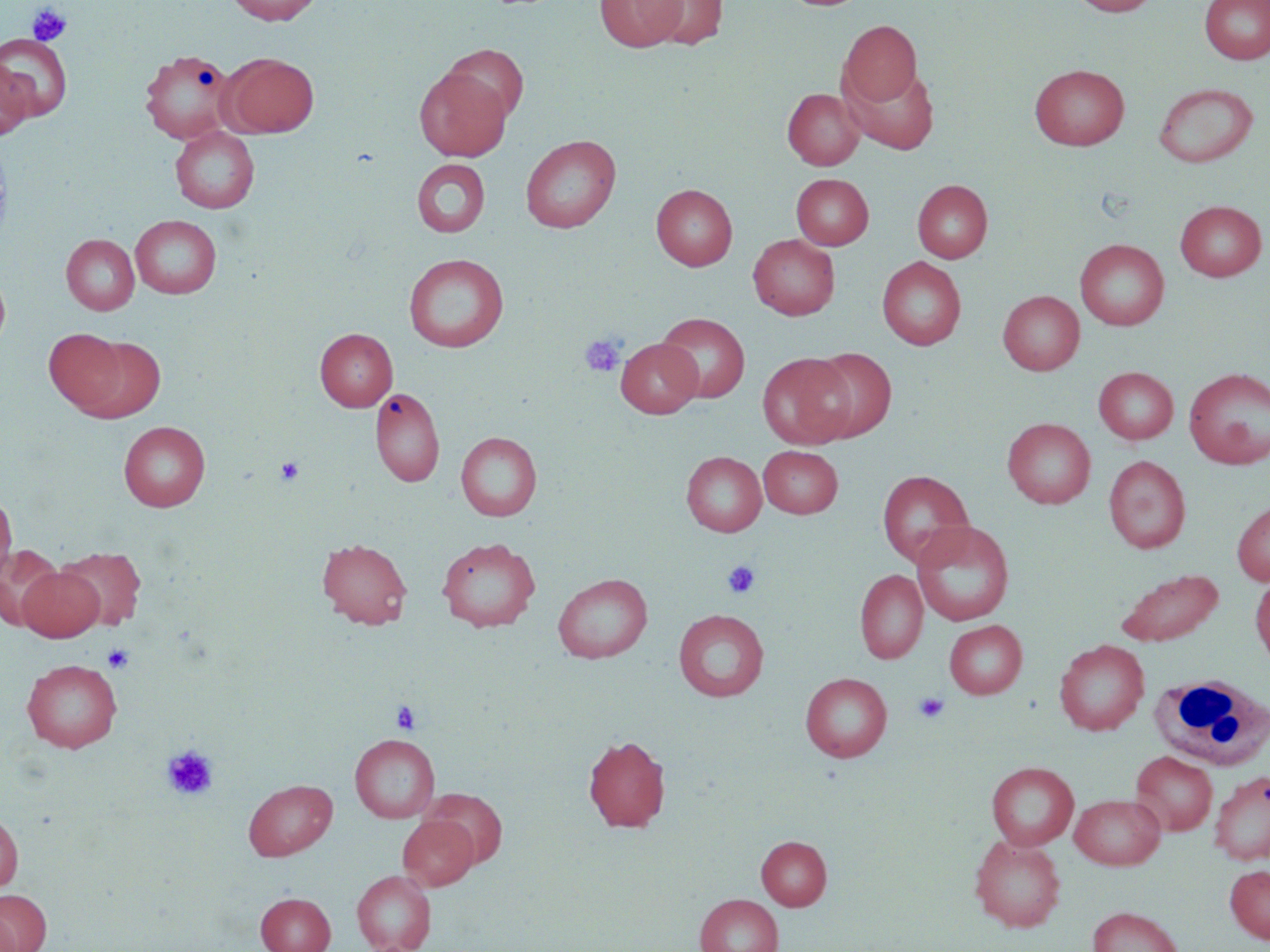

{
  "slide_level_diagnosis": "no evidence of blood parasites",
  "platelet_locations": "approximate bounding boxes as (x1,y1)-(x2,y2) corner pairs in pixels: (27,3)-(71,46), (580,334)-(626,377), (275,457)-(306,485), (722,560)-(761,599), (102,644)-(135,674), (913,692)-(949,724), (391,700)-(421,735), (161,745)-(219,801)",
  "field_of_view": "single",
  "uninfected_red_blood_cell_locations": "approximate bounding boxes as (x1,y1)-(x2,y2) corner pairs in pixels: (226,0)-(323,25), (643,0)-(728,49), (1068,0)-(1160,16), (1200,0)-(1270,64), (596,1)-(685,51), (838,19)-(922,110), (0,34)-(73,120), (442,43)-(529,124), (139,49)-(236,145), (221,53)-(319,137), (0,60)-(34,140), (1029,64)-(1129,151), (843,65)-(940,155), (414,67)-(511,161), (1154,82)-(1258,167), (783,88)-(864,170), (170,127)-(259,213), (520,134)-(621,233), (411,159)-(490,237), (791,174)-(874,249), (912,179)-(993,263), (651,184)-(737,271), (1175,200)-(1267,281), (130,215)-(222,299), (61,233)-(140,315), (748,234)-(840,320), (1074,238)-(1170,330), (403,253)-(509,352), (877,256)-(966,350), (0,269)-(11,353), (998,290)-(1084,375), (656,313)-(750,403), (45,327)-(127,415), (315,327)-(397,411), (77,336)-(166,422), (615,338)-(702,418), (808,347)-(897,442), (758,352)-(855,448), (1093,366)-(1178,444), (1183,368)-(1270,469), (370,386)-(445,487), (1002,417)-(1095,508), (119,421)-(209,511), (455,431)-(542,521), (758,446)-(843,518), (680,451)-(767,536), (1104,455)-(1190,553), (877,470)-(973,568), (0,491)-(17,583), (1232,500)-(1270,586), (911,520)-(1015,626), (436,537)-(541,632), (317,538)-(413,629), (0,546)-(65,629), (55,546)-(146,630), (18,565)-(104,641), (1115,568)-(1224,647), (855,569)-(928,664), (552,573)-(653,663), (1250,574)-(1270,667), (673,609)-(769,701), (944,620)-(1027,699), (1054,639)-(1149,735), (22,659)-(122,752), (800,672)-(892,762), (349,734)-(440,822), (583,734)-(670,832), (1130,750)-(1218,835), (986,761)-(1079,850), (1209,770)-(1270,865), (243,779)-(337,860), (421,788)-(508,867), (1070,793)-(1165,869), (0,811)-(23,892), (397,815)-(479,890), (970,834)-(1066,932), (757,836)-(831,910), (1225,864)-(1270,943), (353,869)-(436,952), (0,889)-(52,952), (256,892)-(335,952), (695,893)-(783,952), (1087,906)-(1184,952)",
  "magnification": "1000x",
  "preparation": "thin blood smear",
  "stain": "May-Grünwald-Giemsa",
  "image_size": "1270×952 pixels",
  "modality": "optical microscopy",
  "white_blood_cell_locations": "approximate bounding boxes as (x1,y1)-(x2,y2) corner pairs in pixels: (1149,673)-(1270,770)"
}